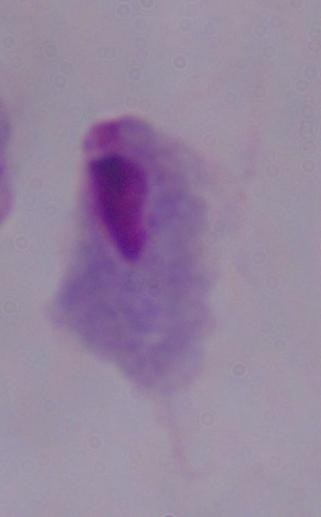 A trichomonad is seen. Micrograph. 1000x magnification.